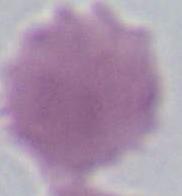

Summary:
  - Identification: red blood cell
  - Magnification: 1000x
  - Modality: photomicrograph